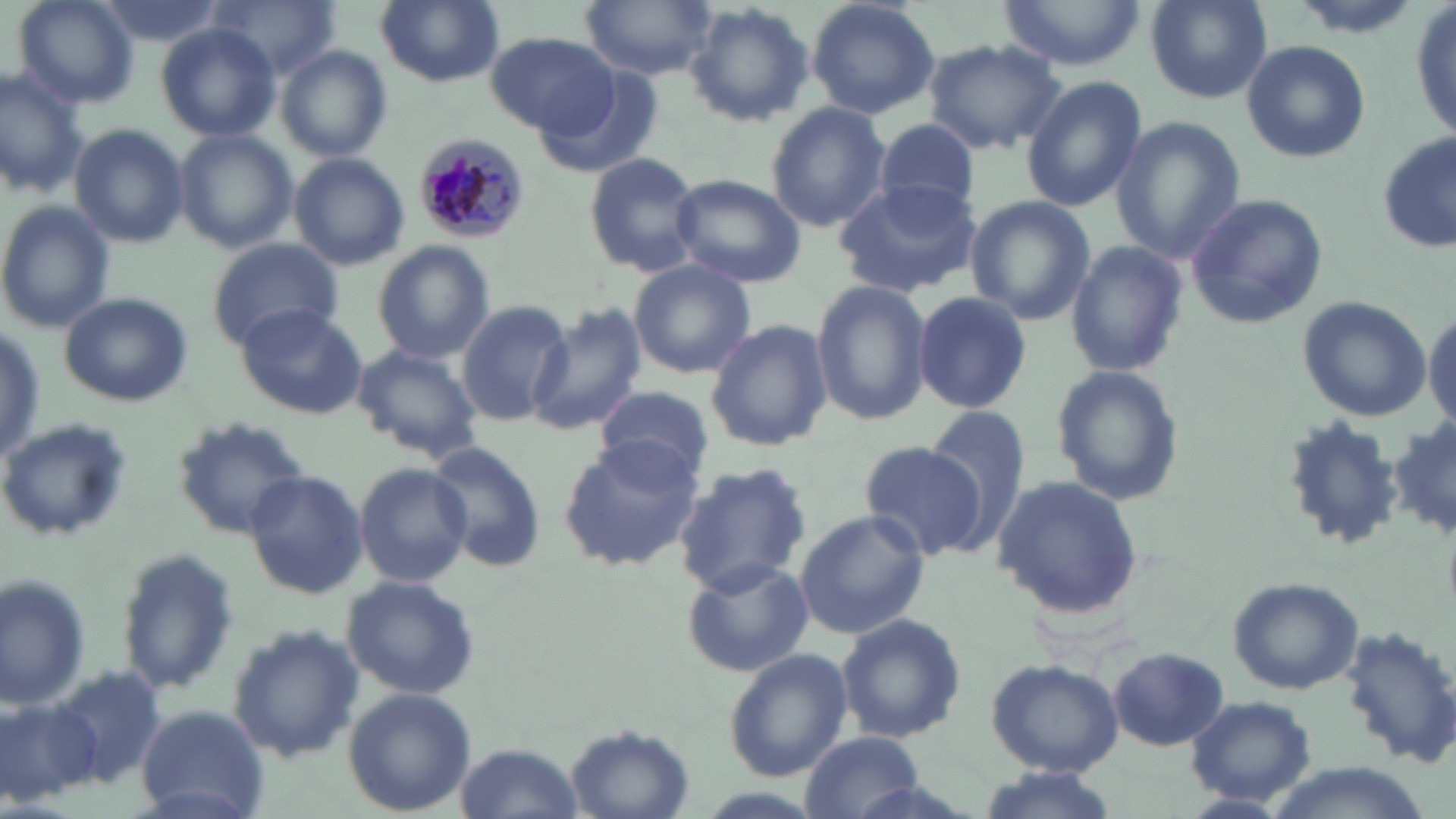
slide-level diagnosis = Plasmodium malariae
preparation = thin blood smear
image size = 1456×819 pixels
uninfected red blood cell locations = approximate bounding boxes as [x1, y1, x2, y2] in pixels: [11, 0, 139, 109], [95, 0, 223, 50], [375, 0, 504, 87], [581, 0, 718, 79], [804, 0, 940, 119], [999, 0, 1146, 71], [1144, 0, 1274, 105], [1408, 0, 1455, 147], [213, 2, 338, 81], [683, 4, 815, 128], [152, 23, 280, 141], [485, 32, 621, 135], [922, 39, 1064, 153], [1241, 40, 1371, 163], [278, 47, 393, 163], [0, 63, 88, 199], [537, 69, 665, 181], [1021, 76, 1146, 212], [766, 102, 890, 232], [1111, 118, 1244, 267], [867, 120, 984, 217], [69, 124, 190, 248], [176, 130, 298, 253], [1376, 133, 1456, 253], [290, 152, 409, 271], [583, 153, 702, 277], [667, 173, 805, 288], [833, 180, 983, 297], [1183, 193, 1330, 327], [964, 196, 1095, 325], [0, 201, 115, 332], [208, 237, 342, 346], [1064, 239, 1188, 379], [373, 241, 494, 364], [626, 260, 756, 378], [809, 279, 932, 425], [913, 291, 1031, 414], [57, 292, 194, 407], [1296, 295, 1432, 422], [457, 300, 574, 426], [232, 304, 368, 420], [1424, 304, 1456, 435], [527, 306, 650, 437], [705, 319, 833, 451], [0, 322, 47, 467], [350, 343, 482, 463], [1050, 365, 1186, 507], [596, 385, 715, 484], [923, 407, 1029, 538], [2, 416, 134, 541], [1391, 417, 1455, 542], [170, 418, 311, 542], [557, 438, 704, 571], [426, 441, 547, 574], [859, 441, 986, 560], [353, 462, 472, 588], [671, 462, 811, 595], [244, 469, 369, 600], [991, 475, 1143, 618], [795, 510, 929, 639], [118, 550, 238, 693], [678, 557, 814, 676], [1, 573, 93, 709], [340, 574, 482, 699], [1227, 576, 1366, 694], [835, 612, 968, 744], [1341, 622, 1456, 765], [228, 625, 366, 762], [723, 648, 851, 782], [1108, 648, 1229, 751], [986, 659, 1124, 776], [43, 667, 168, 790], [342, 685, 476, 816], [0, 692, 104, 806], [1184, 695, 1319, 805], [135, 707, 268, 813], [565, 724, 694, 819], [801, 732, 924, 818], [456, 742, 581, 817], [970, 765, 1122, 818]
field of view = one of a larger specimen
stain = May-Grünwald-Giemsa
magnification = 1000x
modality = optical microscopy
Plasmodium malariae-infected red blood cell locations = approximate bounding boxes as [x1, y1, x2, y2] in pixels: [411, 133, 532, 246]